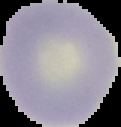

Malaria status: uninfected. From a thin blood film. Image is 121×127 pixels. The area outside the segmented cell region is set to black.